Identify the preparation type.
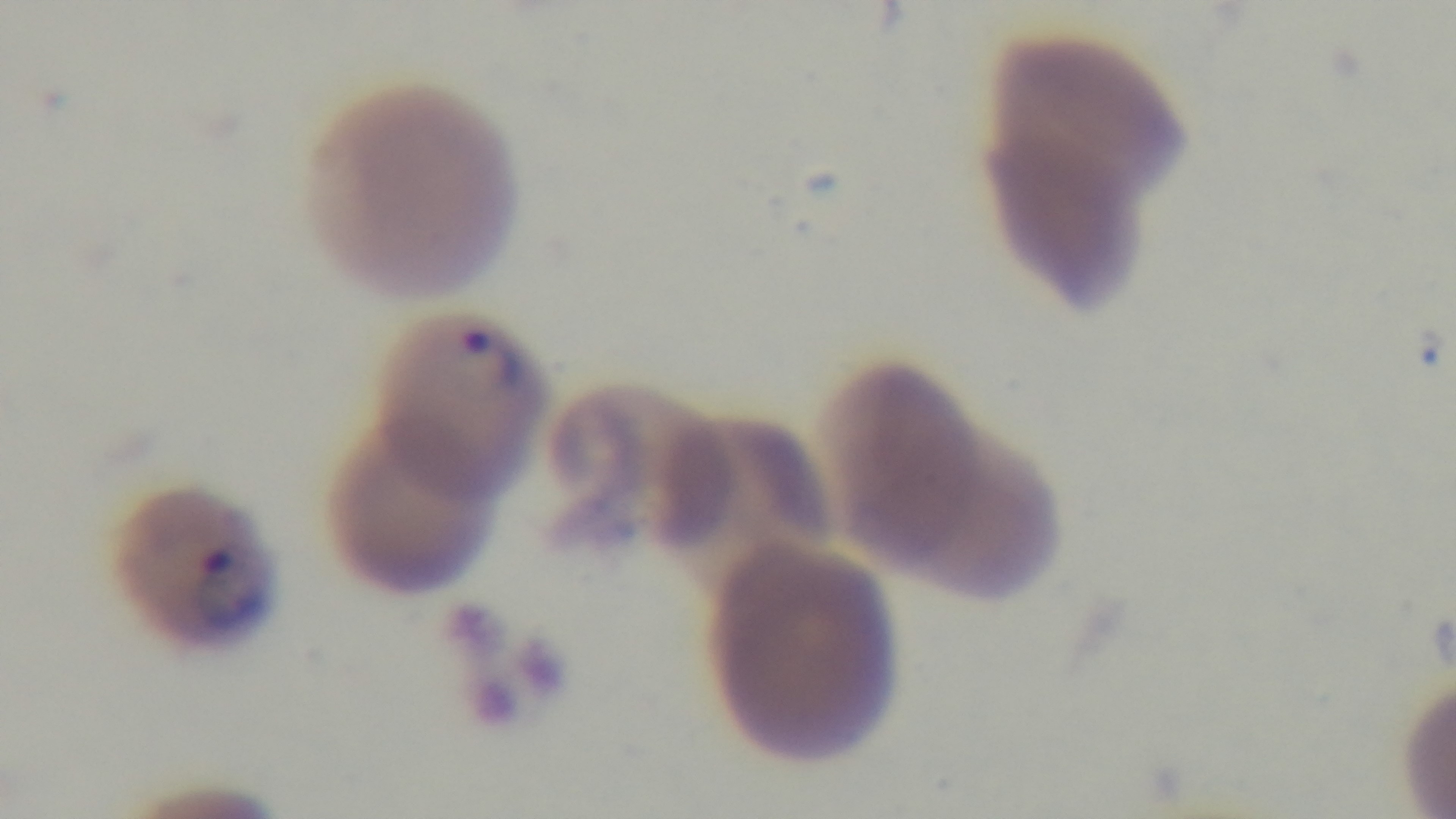
A thin smear.

{
  "stain": "Giemsa",
  "field_of_view": "single",
  "objective": "100x oil immersion",
  "malaria_status": "infected",
  "capture": "mounted 4K digital camera",
  "modality": "light microscopy"
}